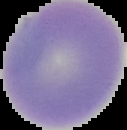

preparation = thin blood smear
image size = 127×130 pixels
image type = segmented cell region with the area outside set to black
malaria status = uninfected